Classify this cell by malaria status.
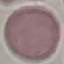
Uninfected.

Summary:
  - Stain: Giemsa
  - Capture: smartphone through the microscope eyepiece
  - Image type: cell patch, automatically extracted from a larger field of view and resized to 64 × 64 pixels
  - Preparation: thin smear